Report the malaria status of this cell.
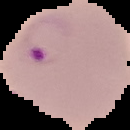

Parasitized.

Summary:
  - Image type: cell region segmented out of the field of view; surrounding area masked to black
  - Image size: 130×130 pixels
  - Preparation: thin blood smear